Assess this cell for malaria.
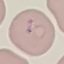

Parasitized.

Giemsa stain. Thin blood smear. Cell patch, automatically extracted from a larger field of view and resized to 64 × 64 pixels. Photographed with a smartphone camera at the microscope eyepiece.